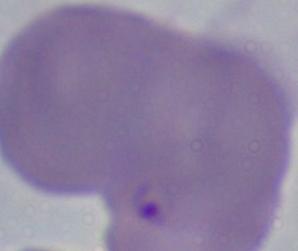
Summary:
  - Identification: Babesia
  - Magnification: 1000x
  - Modality: photomicrograph